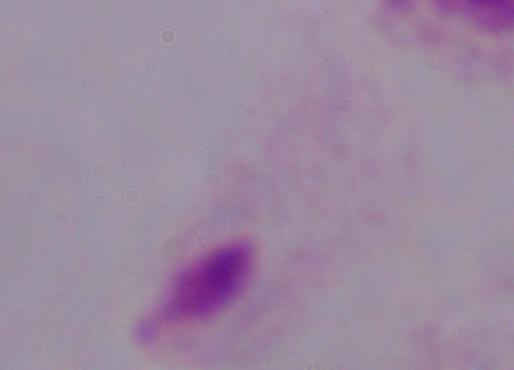

A trichomonad is shown. Photomicrograph. 1000x magnification.